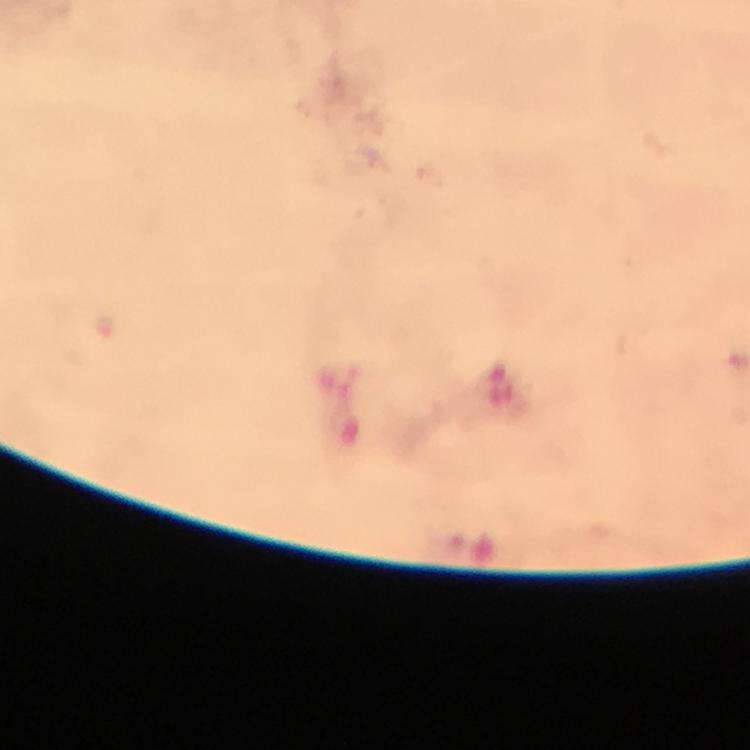 Approximate centers as {x, y} in pixels. Malaria parasite locations: {105, 324}. From a diagnostic examination for malaria. A crop from one field of view. Immersion oil was used. Giemsa stain. Image is 750×750 pixels. Thick blood smear. Photographed with a smartphone mounted on the microscope. 100x magnification.